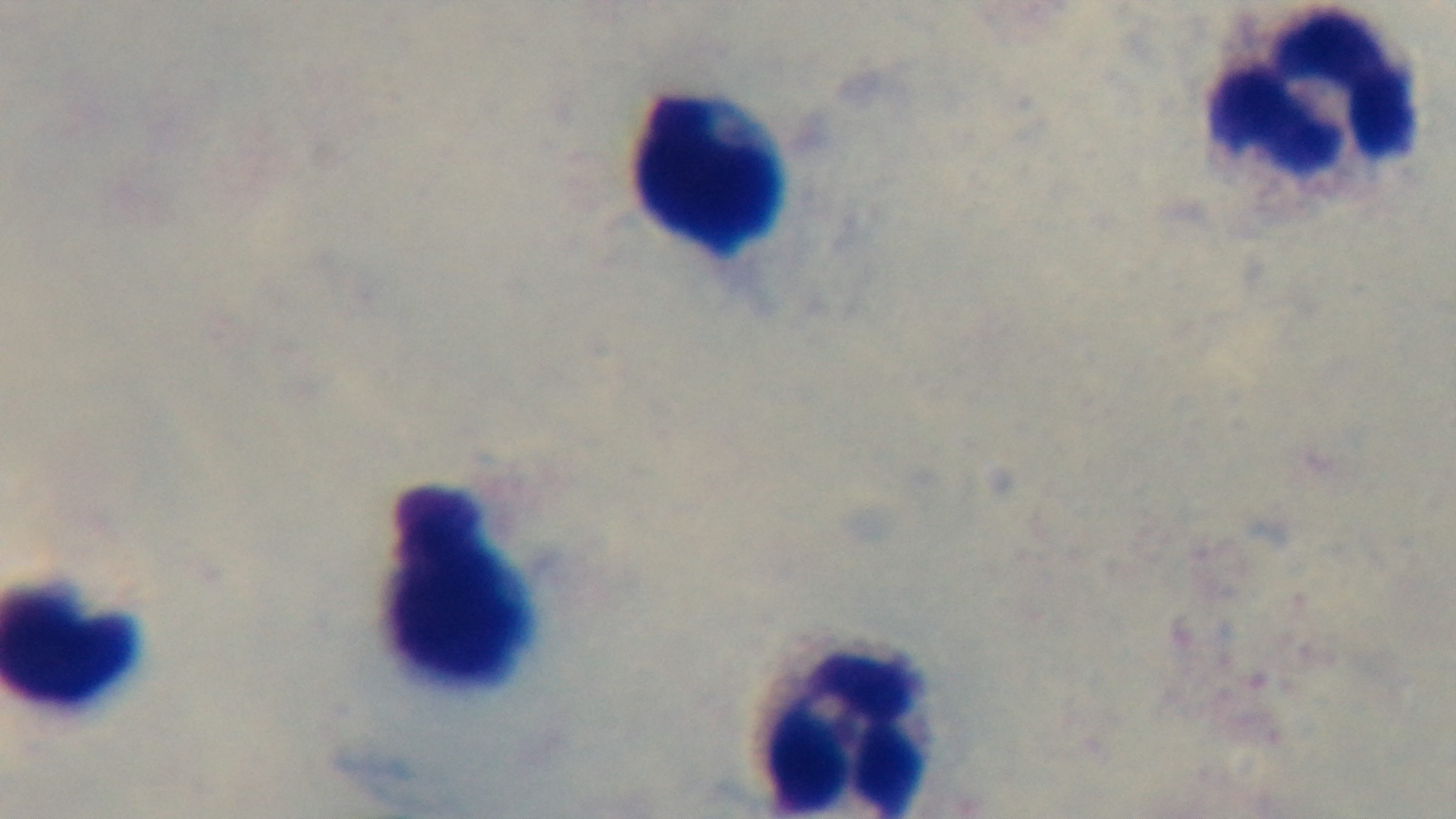

preparation = thick
malaria status = negative
modality = light microscopy
objective = 100x oil immersion
stain = Giemsa
field of view = one from the slide
capture = mounted 4K digital camera